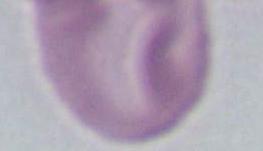
Summary:
  - Identification: red blood cell
  - Modality: photomicrograph
  - Magnification: 1000x